Report the malaria status.
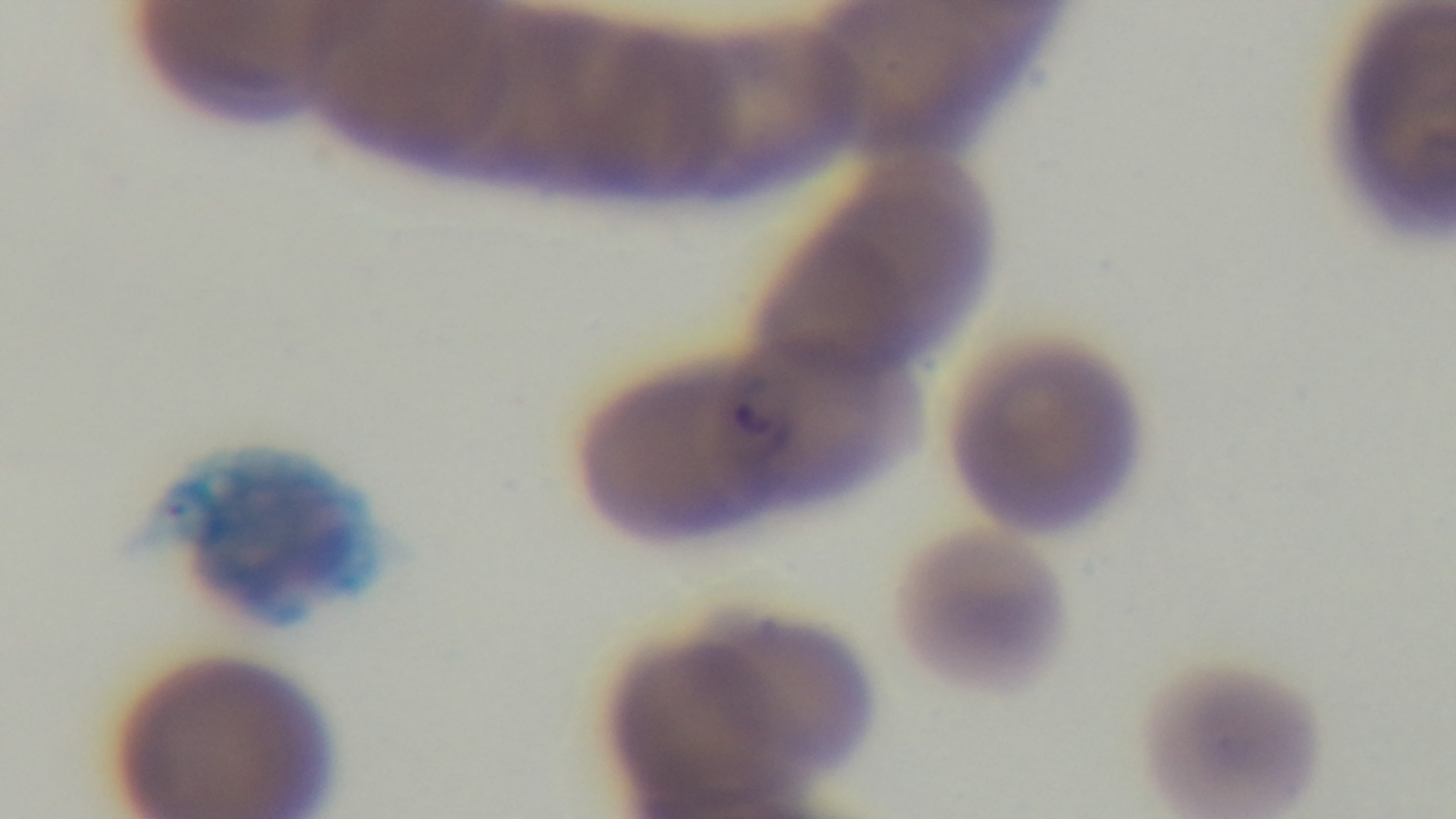
Infected.

One field from the slide. Captured with a mounted 4K digital camera. Photomicrograph. Preparation: thin blood film. Giemsa-stained. 100x oil-immersion objective.